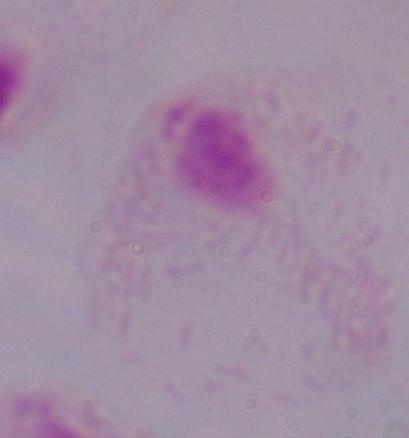

Summary:
  - Identification: trichomonad
  - Modality: photomicrograph
  - Magnification: 1000x